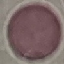
Summary:
  - Malaria status: uninfected
  - Preparation: thin blood film
  - Capture: smartphone camera at the microscope eyepiece
  - Image type: cell patch, automatically extracted from a larger field of view and resized to 64 × 64 pixels
  - Stain: Giemsa